Report the malaria status of this cell.
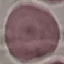

It is uninfected.

preparation: thin smear
image_type: automatically extracted cell patch, resized to 64 × 64 pixels
stain: Giemsa
capture: smartphone through the microscope eyepiece